Give the position of every Plasmodium parasite visible.
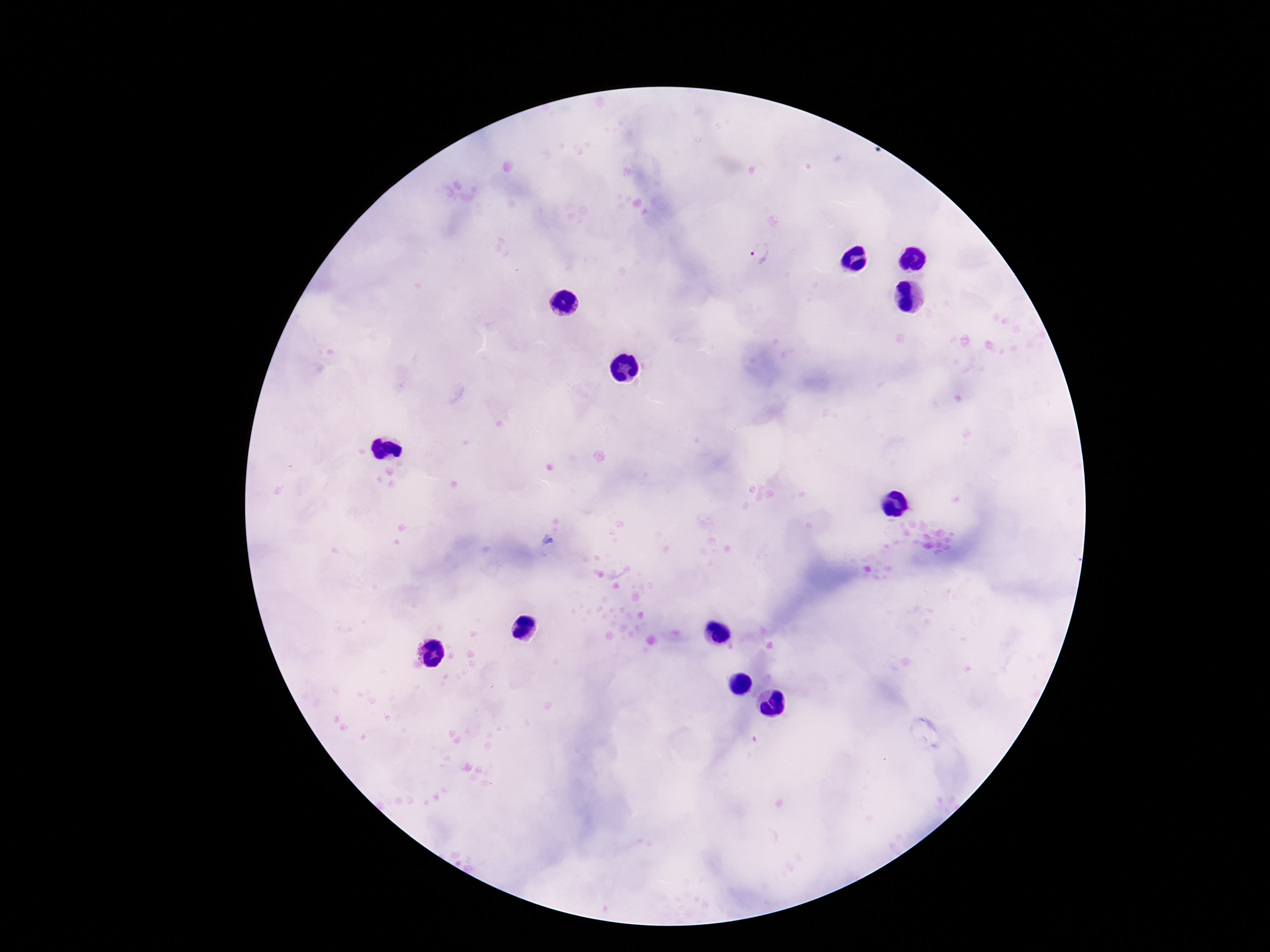
Approximate centers as {x, y} in pixels.
Plasmodium parasites: {762, 258}.

field_of_view: one from this slide
patient_malaria_status: positive
stain: Giemsa
preparation: thick peripheral-blood smear
image_size: 1270×952 pixels
magnification: 100x
capture: smartphone camera through the microscope eyepiece